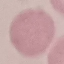

malaria status = uninfected
stain = Giemsa
capture = smartphone through the microscope eyepiece
image type = automatically extracted cell patch, resized to 64 × 64 pixels
preparation = thin blood film